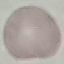

Summary:
  - Result: no malaria parasites seen
  - Stain: Giemsa
  - Capture: smartphone camera at the microscope eyepiece
  - Image type: cell patch, automatically extracted from a larger field of view and resized to 64 × 64 pixels
  - Preparation: thin blood smear